Comment on the morphology of the erythrocytes.
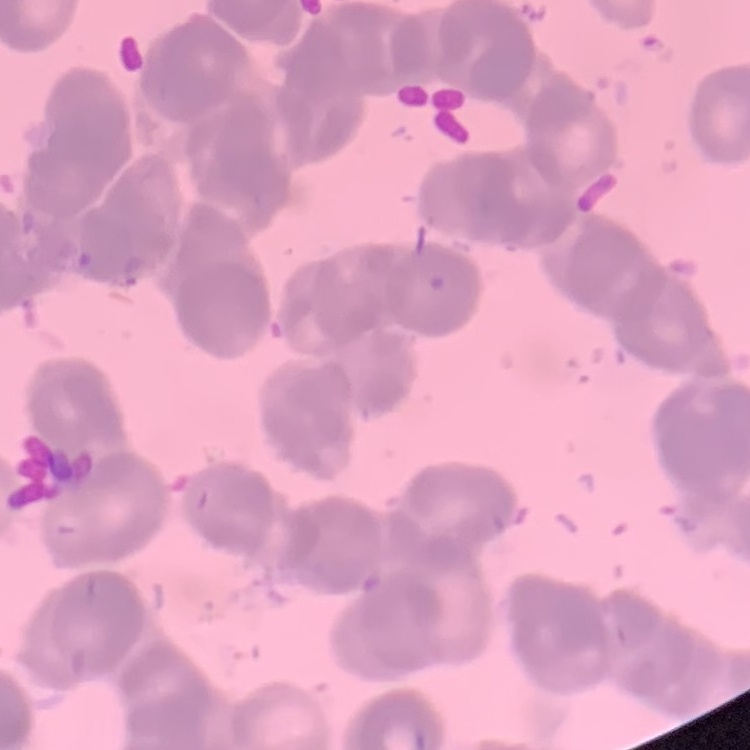

They show rouleaux formation.

Summary:
  - Stain: Field's or Giemsa
  - Image type: square crop of a larger photomicrograph
  - Preparation: thin peripheral smear